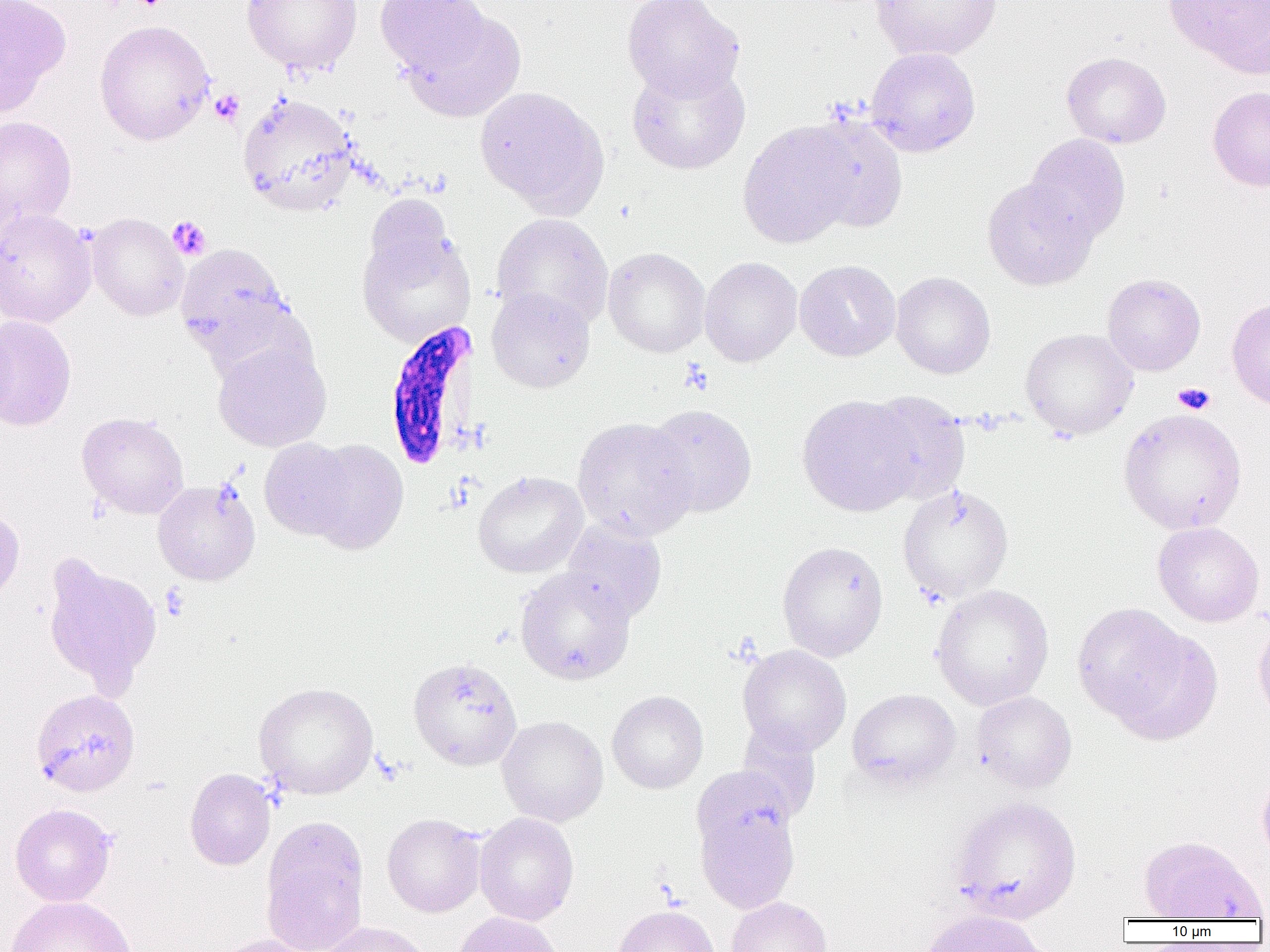
{
  "slide_level_diagnosis": "Plasmodium falciparum",
  "uninfected_red_blood_cell_locations": "approximate bounding boxes as (x1, y1, x2, y2) in pixels: (0, 0, 71, 117), (241, 0, 363, 76), (374, 0, 492, 79), (621, 0, 745, 100), (870, 0, 1002, 62), (1165, 0, 1270, 78), (402, 10, 527, 122), (94, 19, 215, 145), (865, 46, 981, 157), (1061, 51, 1171, 149), (626, 62, 750, 175), (474, 86, 609, 217), (1207, 86, 1270, 191), (237, 92, 359, 216), (800, 114, 909, 234), (0, 116, 77, 232), (737, 120, 861, 249), (1024, 134, 1131, 244), (981, 177, 1098, 291), (363, 194, 456, 288), (0, 208, 97, 328), (87, 212, 188, 321), (491, 213, 614, 332), (357, 227, 477, 346), (175, 243, 294, 359), (603, 247, 710, 357), (699, 256, 802, 367), (795, 260, 901, 361), (891, 271, 996, 379), (1102, 273, 1206, 376), (486, 287, 595, 393), (1226, 298, 1270, 411), (0, 314, 77, 432), (1019, 327, 1139, 440), (212, 340, 332, 451), (862, 391, 970, 505), (796, 394, 921, 517), (645, 404, 757, 517), (1118, 408, 1247, 535), (76, 412, 190, 520), (571, 417, 697, 540), (259, 438, 358, 541), (303, 439, 409, 554), (473, 471, 588, 578), (153, 479, 260, 585), (897, 483, 1014, 602), (0, 506, 24, 602), (561, 520, 667, 624), (1152, 521, 1265, 627), (777, 540, 888, 661), (41, 554, 162, 693), (514, 568, 635, 684), (930, 584, 1054, 710), (1071, 602, 1197, 728), (1253, 616, 1270, 731), (1106, 628, 1223, 746), (738, 644, 851, 756), (408, 656, 523, 771), (253, 682, 378, 799), (30, 688, 140, 797), (847, 688, 960, 790), (607, 691, 708, 794), (971, 691, 1077, 793), (497, 716, 609, 826), (735, 722, 822, 824), (690, 765, 796, 864), (184, 767, 276, 870), (1256, 772, 1270, 868), (949, 796, 1082, 924), (10, 803, 116, 907), (695, 806, 800, 914), (382, 813, 485, 917), (474, 813, 579, 925), (260, 815, 370, 952), (1139, 836, 1265, 921), (3, 895, 137, 952), (725, 897, 833, 952), (612, 904, 720, 952), (917, 909, 1050, 952), (452, 912, 565, 952), (316, 921, 432, 952), (209, 934, 320, 952)",
  "modality": "optical microscopy",
  "platelet_locations": "approximate bounding boxes as (x1, y1, x2, y2) in pixels: (210, 90, 244, 125), (167, 216, 211, 259), (679, 359, 714, 395), (1173, 382, 1216, 415), (160, 583, 190, 621)",
  "field_of_view": "one of a larger specimen",
  "image_size": "1270×952 pixels",
  "preparation": "thin blood smear",
  "plasmodium_falciparum_infected_red_blood_cell_locations": "approximate bounding boxes as (x1, y1, x2, y2) in pixels: (383, 321, 478, 471)",
  "magnification": "1000x"
}